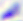

Toxoplasma gondii is seen. Captured at 400x magnification. Photomicrograph.